Assess this cell for malaria.
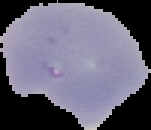

Parasitized.

Summary:
  - Preparation: thin blood film
  - Image type: segmented cell region on a black background
  - Image size: 151×130 pixels